State which parasite is depicted.
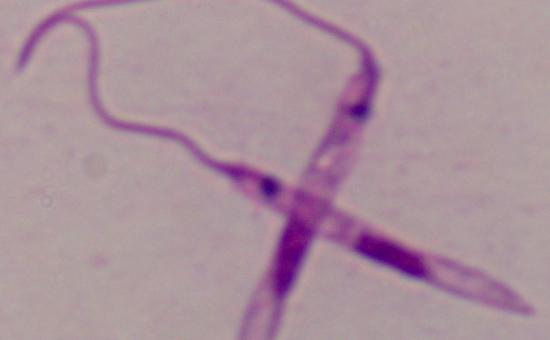

Leishmania.

Summary:
  - Modality: micrograph
  - Magnification: 1000x